State the preparation type.
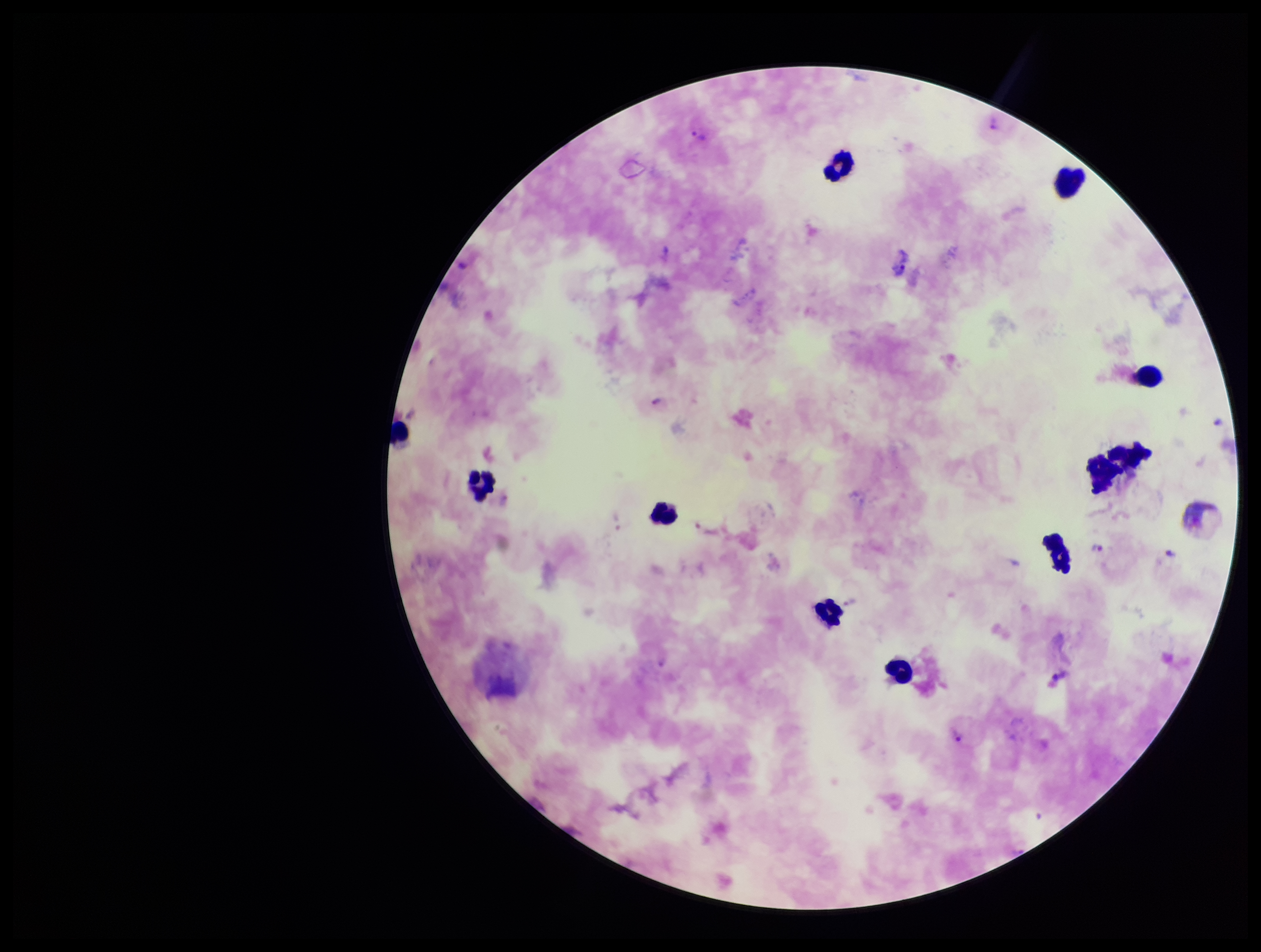

Thick.

field of view = one from this slide
image size = 1261×952 pixels
patient malaria status = infected
capture = smartphone photograph through the microscope eyepiece
stain = Giemsa
Plasmodium parasites = detected
leukocyte count = 11
species reported for this patient = Plasmodium vivax
parasite count = 7